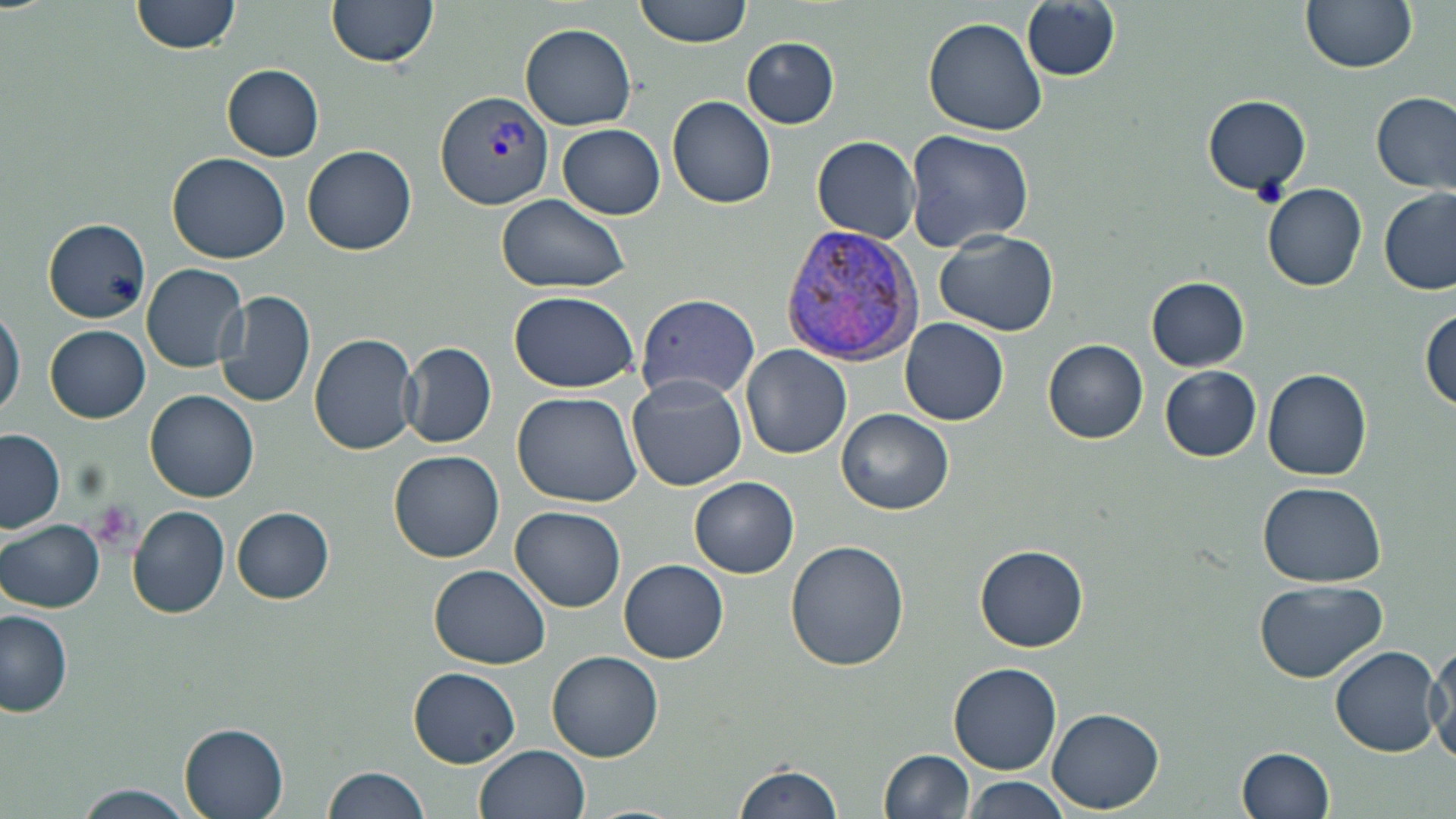
Plasmodium vivax-infected red blood cell locations = approximate bounding boxes as [x1, y1, x2, y2] in pixels: [435, 90, 555, 207], [779, 225, 925, 364]
slide-level diagnosis = Plasmodium vivax
stain = May-Grünwald-Giemsa
modality = light microscopy
field of view = single
image size = 1456×819 pixels
platelet locations = approximate bounding boxes as [x1, y1, x2, y2] in pixels: [1252, 176, 1290, 209], [90, 503, 141, 553]
uninfected red blood cell locations = approximate bounding boxes as [x1, y1, x2, y2] in pixels: [131, 0, 244, 56], [327, 0, 437, 69], [631, 0, 756, 47], [1300, 0, 1417, 74], [1022, 2, 1120, 82], [922, 17, 1046, 136], [519, 23, 638, 130], [741, 37, 839, 128], [222, 65, 325, 161], [1372, 91, 1455, 193], [1203, 95, 1312, 195], [667, 96, 776, 209], [557, 125, 665, 219], [905, 130, 1035, 251], [811, 135, 921, 243], [302, 144, 418, 255], [167, 152, 292, 262], [1262, 183, 1367, 291], [1378, 186, 1455, 296], [497, 194, 629, 294], [43, 219, 150, 321], [935, 230, 1058, 336], [141, 263, 247, 371], [1146, 276, 1250, 370], [219, 289, 317, 410], [509, 290, 640, 393], [637, 293, 762, 402], [0, 303, 23, 422], [1421, 309, 1455, 414], [901, 318, 1009, 425], [45, 325, 150, 423], [309, 332, 421, 456], [1044, 339, 1149, 443], [401, 342, 496, 449], [741, 344, 850, 458], [1262, 365, 1372, 481], [1159, 366, 1263, 462], [627, 375, 748, 491], [146, 390, 259, 503], [512, 391, 644, 507], [838, 407, 954, 514], [0, 429, 65, 533], [388, 450, 504, 562], [689, 474, 800, 578], [1257, 481, 1386, 584], [128, 505, 230, 619], [511, 505, 625, 612], [232, 507, 334, 604], [0, 518, 105, 611], [785, 539, 910, 670], [974, 545, 1089, 652], [620, 560, 728, 663], [430, 564, 550, 669], [1253, 579, 1387, 683], [0, 609, 73, 717], [1429, 644, 1456, 769], [1329, 647, 1441, 758], [548, 650, 664, 762], [949, 662, 1062, 773], [408, 668, 520, 766], [1048, 707, 1164, 812], [179, 722, 291, 819], [477, 744, 591, 819], [1237, 745, 1334, 817], [880, 750, 974, 819], [731, 761, 843, 819], [324, 765, 432, 819], [957, 778, 1073, 818], [76, 784, 193, 819]
magnification = 1000x
preparation = thin blood film